State the blood parasite species.
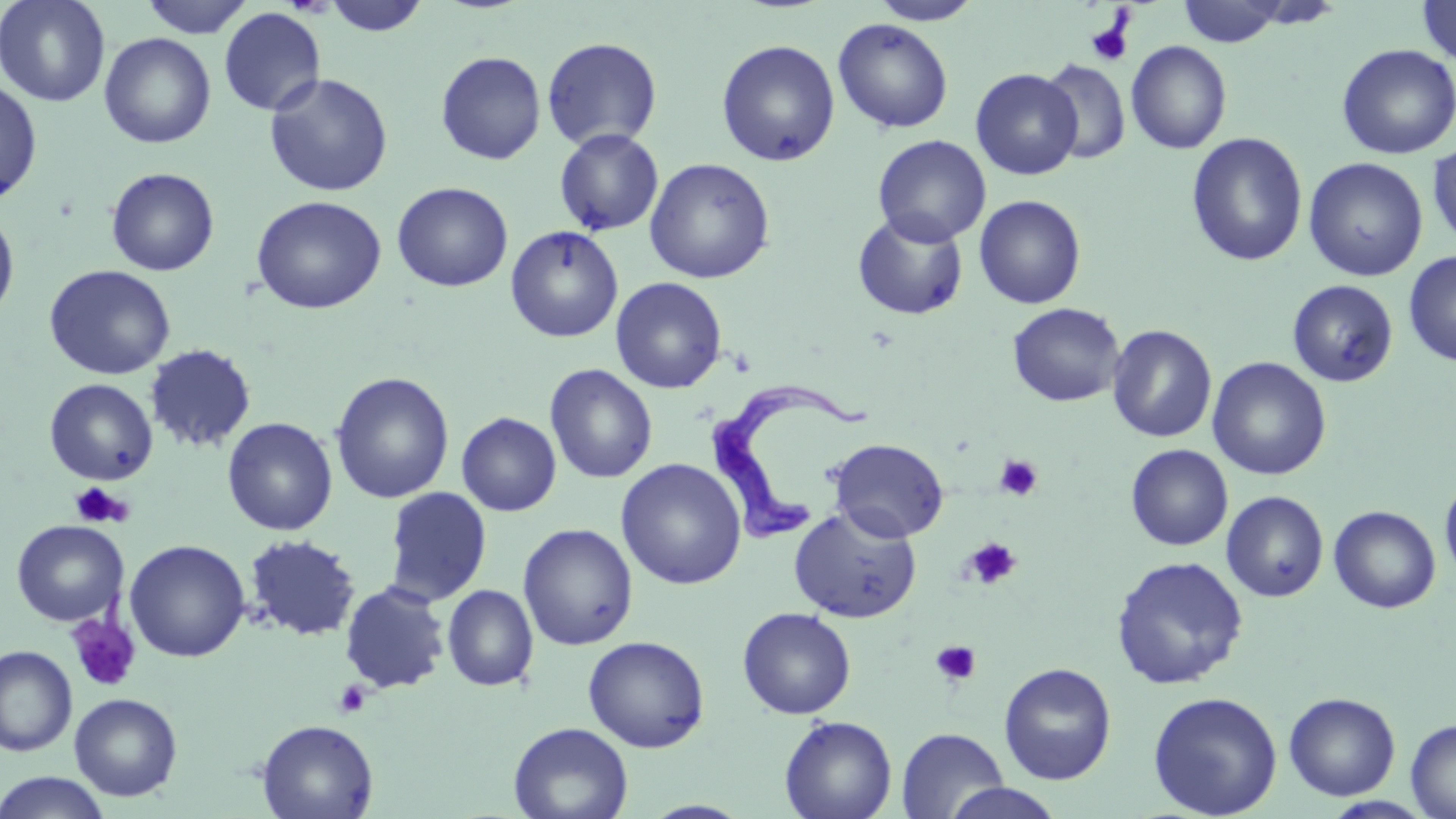
Trypanosoma brucei.

platelet locations = approximate bounding boxes as (x1,y1)-(x2,y2) corner pairs in pixels: (1086,17)-(1134,66), (994,455)-(1044,501), (69,482)-(131,528), (963,537)-(1022,590), (66,615)-(141,693), (930,640)-(982,687), (333,680)-(371,717)
modality = light microscopy
image size = 1456×819 pixels
magnification = 1000x
preparation = thin blood smear
stain = May-Grünwald-Giemsa
uninfected red blood cell locations = approximate bounding boxes as (x1,y1)-(x2,y2) corner pairs in pixels: (0,0)-(111,107), (138,0)-(256,38), (321,0)-(431,37), (868,0)-(984,25), (1176,0)-(1291,48), (1416,0)-(1456,66), (218,7)-(326,117), (833,18)-(954,134), (99,32)-(216,148), (541,37)-(663,151), (716,39)-(840,167), (1126,40)-(1232,154), (1336,43)-(1456,159), (435,51)-(545,165), (1040,59)-(1131,164), (970,68)-(1082,180), (264,73)-(393,197), (0,79)-(42,204), (900,117)-(1029,227), (553,128)-(664,236), (1186,132)-(1308,268), (873,134)-(991,247), (1427,141)-(1456,249), (1303,157)-(1428,281), (644,158)-(775,284), (105,167)-(220,276), (391,182)-(513,292), (251,195)-(386,315), (974,195)-(1086,309), (0,206)-(20,323), (852,210)-(969,321), (505,225)-(624,342), (1403,250)-(1456,367), (44,264)-(175,380), (610,277)-(727,394), (1287,280)-(1398,387), (1007,302)-(1125,407), (1106,324)-(1217,443), (145,344)-(256,453), (1207,357)-(1331,480), (545,364)-(658,484), (330,372)-(454,504), (44,379)-(158,485), (456,412)-(562,516), (222,417)-(338,536), (827,438)-(949,543), (1125,444)-(1233,550), (615,458)-(747,590), (1439,474)-(1456,584), (384,486)-(492,606), (1221,490)-(1328,602), (1329,505)-(1441,613), (789,506)-(922,623), (11,520)-(127,626), (518,523)-(638,650), (244,534)-(360,641), (124,539)-(251,662), (1110,555)-(1249,690), (339,581)-(450,694), (442,584)-(539,692), (737,607)-(856,719), (583,635)-(710,753), (0,645)-(77,757), (998,662)-(1117,785), (1147,691)-(1283,819), (1283,692)-(1400,801), (69,693)-(183,801), (779,715)-(898,819), (1406,718)-(1455,818), (257,719)-(378,818), (508,722)-(634,819), (896,728)-(1009,818), (0,771)-(112,818), (941,783)-(1067,819)
field of view = one of a larger specimen
Trypanosoma brucei locations = approximate bounding boxes as (x1,y1)-(x2,y2) corner pairs in pixels: (704,374)-(881,557)